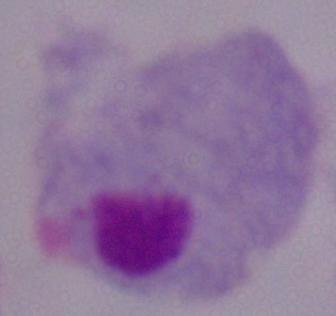
{
  "magnification": "1000x",
  "modality": "photomicrograph",
  "identification": "trichomonad"
}